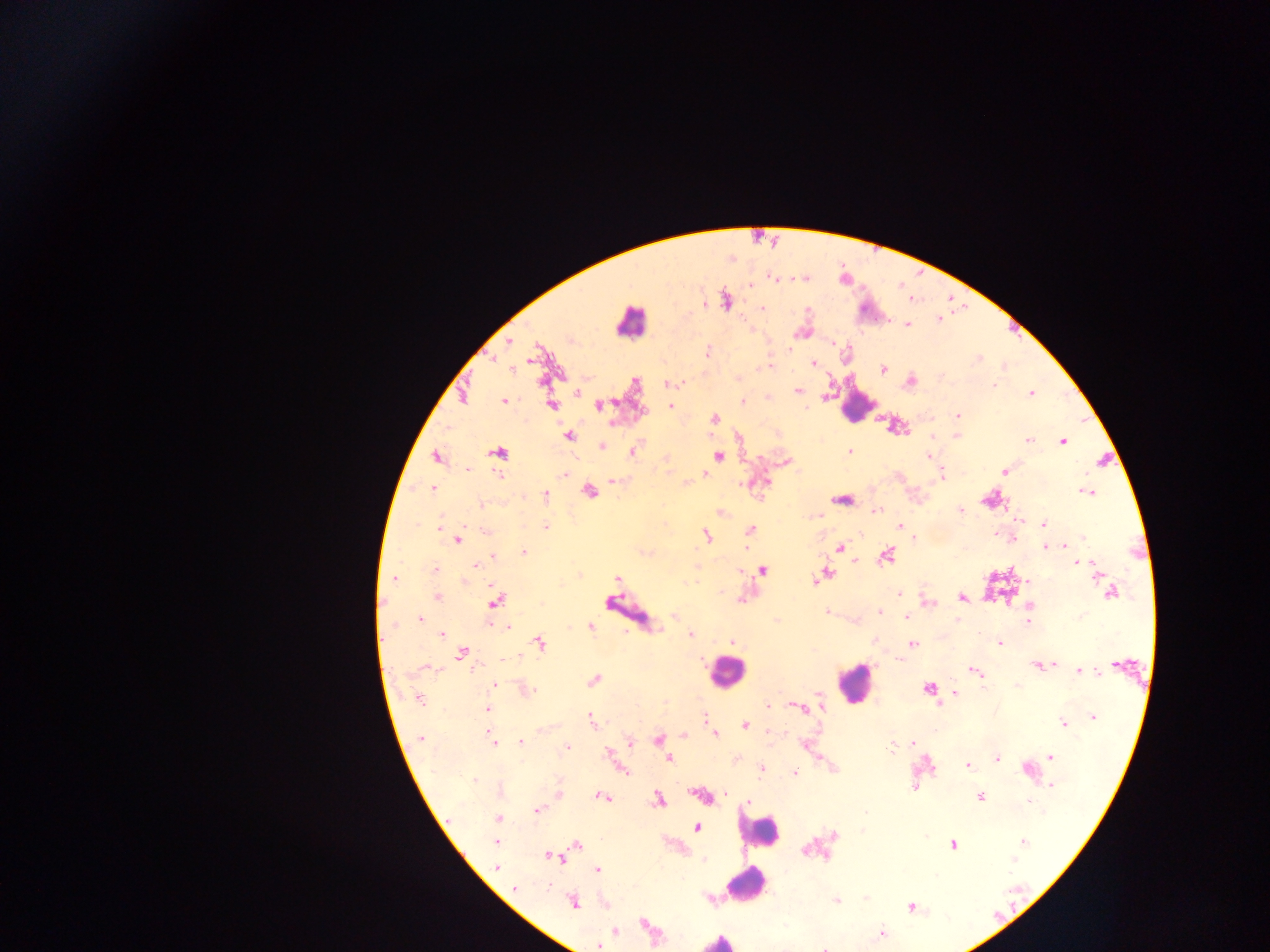
Approximate centers as x y in pixels.
Summary:
  - Leukocyte locations: 630 322; 856 404; 726 672; 855 682; 758 832; 747 883; 719 941
  - Malaria parasite locations: 772 278; 726 301; 704 304; 763 308; 939 320; 908 325; 509 342; 790 349; 708 353; 977 359; 814 363; 770 366; 512 369; 883 369; 909 382; 669 383; 994 386; 798 390; 578 393; 1031 394; 504 401; 742 402; 551 405; 599 405; 670 406; 958 415; 714 419; 568 436; 957 436; 932 437; 1029 440; 1062 441; 602 446; 633 451; 850 451; 498 453; 718 456; 927 456; 436 457; 786 462; 467 469; 1005 471; 565 474; 706 475; 500 476; 942 476; 613 481; 433 489; 588 492; 1087 492; 545 494; 841 499; 482 505; 876 510; 961 510; 721 512; 1019 520; 1044 524; 900 526; 440 527; 545 527; 486 530; 750 530; 995 534; 706 536; 1001 536; 1083 537; 458 539; 1012 539; 1045 547; 1066 547; 840 548; 524 553; 886 556; 494 557; 855 562; 1079 563; 1091 564; 477 565; 434 570; 762 570; 826 574; 395 578; 617 579; 814 581; 1111 592; 898 593; 437 597; 961 598; 496 601; 928 603; 1029 606; 826 611; 879 612; 674 616; 906 617; 420 619; 957 620; 1028 621; 507 626; 590 626; 441 634; 691 634; 732 642; 1000 642; 540 643; 913 644; 461 654; 505 659; 901 659; 1051 665; 1036 666; 425 667; 974 670; 1079 671; 593 680; 494 685; 1018 685; 983 688; 928 689; 526 690; 955 693; 419 700; 768 706; 821 707; 801 708; 488 709; 1093 717; 704 719; 591 720; 1063 723; 745 725; 716 734; 684 736; 421 738; 492 739; 658 739; 521 742; 631 742; 913 744; 804 745; 566 747; 893 747; 664 752; 608 754; 1051 756; 668 759; 998 759; 735 760; 968 765; 762 770; 1027 770; 624 771; 795 773; 474 780; 1052 786; 915 787; 559 793; 726 794; 700 795; 602 797; 980 797; 658 800; 749 801; 1030 801; 538 810; 498 818; 696 828; 496 842; 1023 842; 954 844; 577 845; 550 857; 704 859; 1012 859; 497 867; 597 871; 515 888; 866 897; 837 901; 573 902; 911 907; 644 924; 616 931; 882 934; 598 946; 824 948
  - Country: Ghana
  - Image size: 1270×952 pixels
  - Preparation: thick blood film
  - Capture: mobile-phone photograph through a microscope
  - Field of view: single